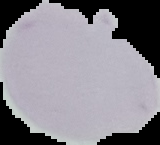 From a thin blood film. The area outside the segmented cell region is set to black. Image is 160×145 pixels. Malaria status: uninfected.